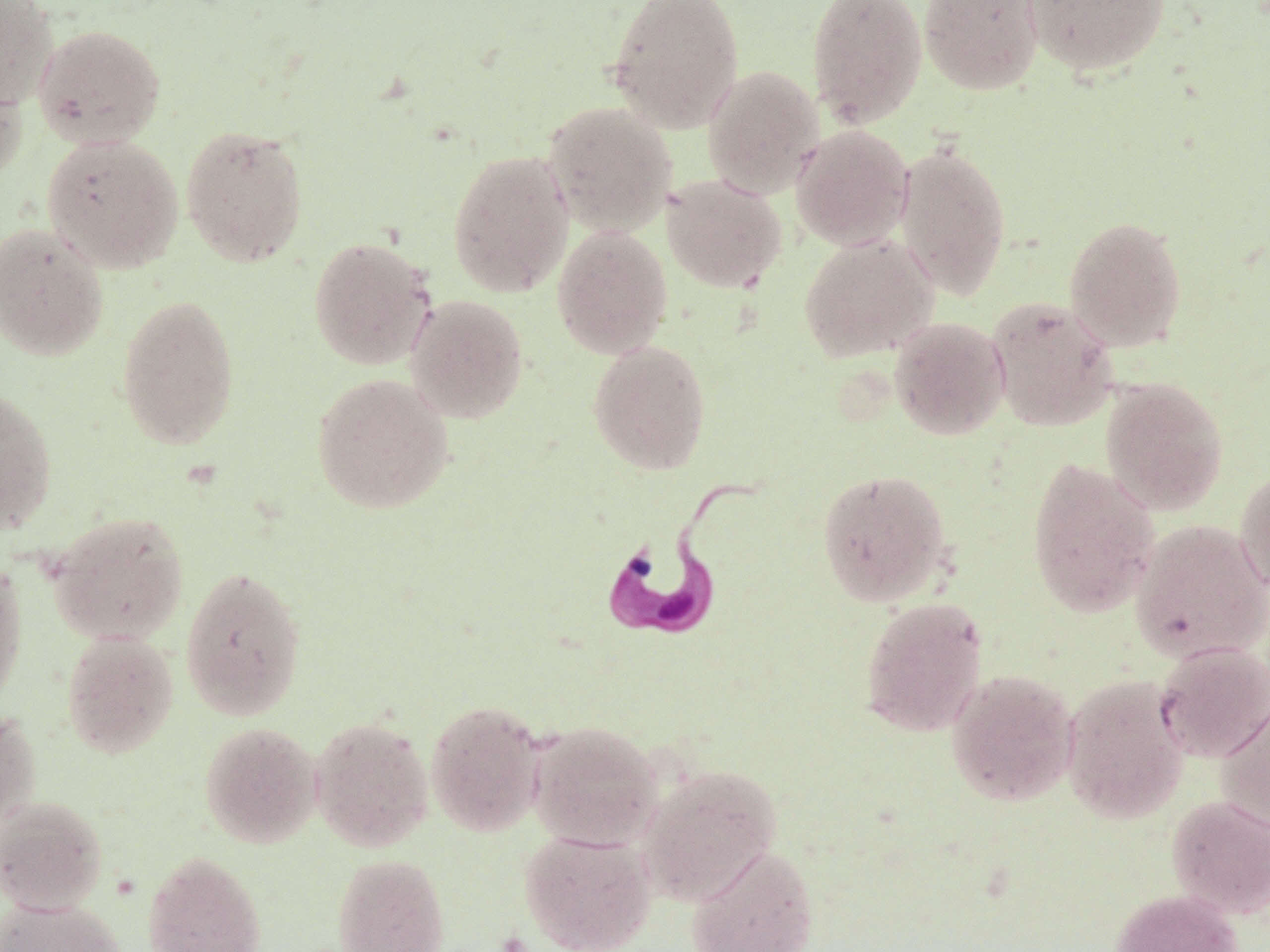
Summary:
  - Coordinate format: approximate bounding boxes as [x1, y1, x2, y2] in pixels
  - Trypanosoma brucei locations: [595, 468, 766, 645]
  - Uninfected red blood cell locations: [0, 0, 59, 110], [606, 0, 745, 134], [806, 0, 927, 129], [918, 0, 1044, 96], [1022, 0, 1170, 77], [32, 23, 166, 150], [0, 61, 28, 190], [702, 65, 824, 199], [542, 101, 677, 236], [180, 124, 309, 268], [790, 125, 914, 250], [41, 133, 184, 273], [893, 141, 1012, 301], [447, 149, 574, 298], [662, 174, 787, 293], [1064, 215, 1188, 352], [0, 221, 109, 362], [552, 225, 673, 359], [798, 233, 938, 363], [308, 235, 437, 370], [115, 293, 240, 451], [405, 294, 529, 424], [986, 296, 1118, 432], [889, 316, 1010, 440], [587, 339, 712, 474], [311, 373, 454, 514], [1100, 377, 1229, 515], [0, 386, 57, 536], [1027, 458, 1160, 618], [1235, 466, 1270, 596], [817, 468, 953, 607], [47, 511, 189, 645], [1131, 519, 1270, 663], [0, 555, 27, 711], [179, 564, 307, 721], [859, 596, 989, 737], [61, 630, 179, 758], [1153, 642, 1270, 763], [945, 668, 1079, 806], [1060, 674, 1190, 824], [1215, 696, 1270, 836], [425, 698, 547, 837], [0, 706, 41, 830], [310, 715, 434, 852], [527, 720, 664, 850], [199, 721, 322, 849], [636, 762, 783, 905], [1165, 794, 1270, 919], [0, 795, 108, 915], [518, 829, 657, 952], [685, 844, 819, 952], [142, 851, 267, 952], [331, 853, 450, 952], [1111, 888, 1243, 952], [0, 897, 127, 952]
  - Slide-level diagnosis: Trypanosoma brucei
  - Stain: May-Grünwald-Giemsa
  - Preparation: thin blood film
  - Modality: light microscopy
  - Field of view: one of a larger specimen
  - Image size: 1270×952 pixels
  - Magnification: 1000x